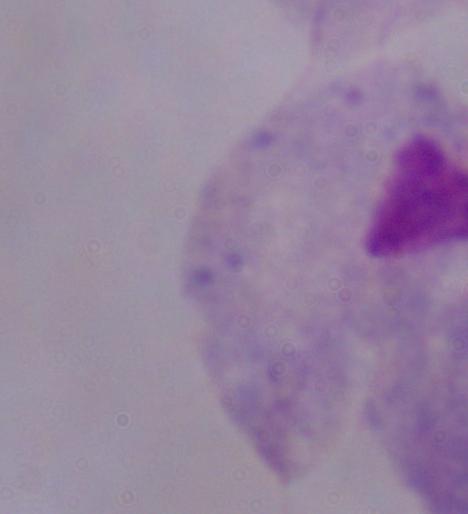
modality: micrograph
magnification: 1000x
identification: trichomonad